Locate every blood parasite and identify its species.
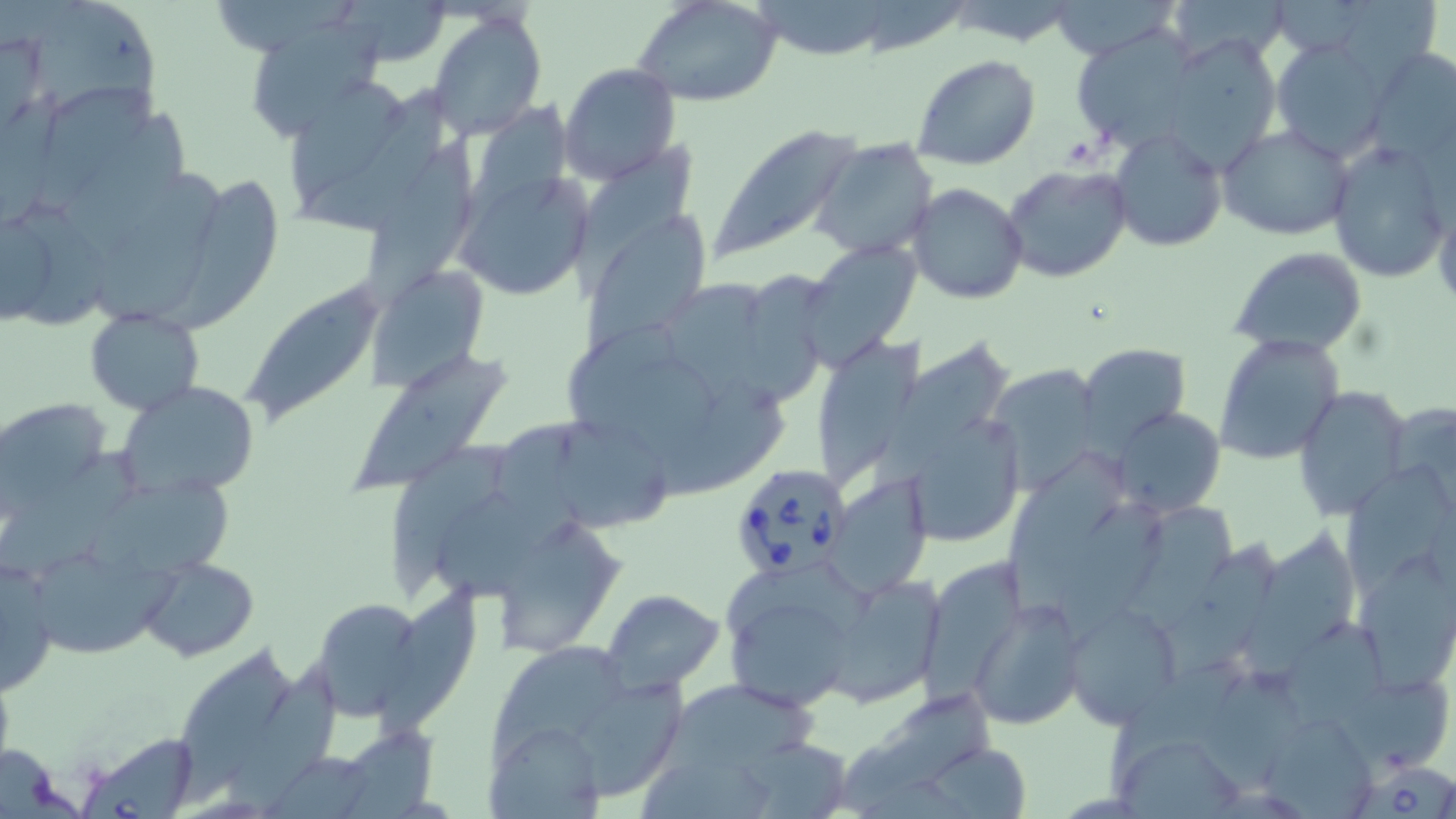
Approximate bounding boxes as named x1/y1/x2/y2 corners in pixels.
Babesia divergens-infected red blood cells: (x1=726, y1=460, x2=856, y2=579), (x1=76, y1=733, x2=201, y2=817), (x1=1354, y1=763, x2=1456, y2=819).
No Plasmodium falciparum, Plasmodium ovale, Plasmodium malariae, Plasmodium vivax, or Trypanosoma brucei observed.

Uninfected red blood cell locations: (x1=342, y1=0, x2=455, y2=68), (x1=1052, y1=0, x2=1176, y2=58), (x1=1164, y1=0, x2=1293, y2=65), (x1=1347, y1=0, x2=1440, y2=91), (x1=758, y1=1, x2=890, y2=65), (x1=1276, y1=1, x2=1370, y2=55), (x1=635, y1=2, x2=784, y2=108), (x1=213, y1=3, x2=365, y2=52), (x1=29, y1=9, x2=169, y2=129), (x1=428, y1=10, x2=546, y2=139), (x1=252, y1=20, x2=394, y2=149), (x1=1070, y1=29, x2=1202, y2=154), (x1=1162, y1=33, x2=1283, y2=173), (x1=1270, y1=37, x2=1392, y2=161), (x1=1366, y1=48, x2=1455, y2=163), (x1=911, y1=54, x2=1040, y2=171), (x1=559, y1=63, x2=682, y2=187), (x1=292, y1=81, x2=410, y2=210), (x1=306, y1=83, x2=456, y2=240), (x1=38, y1=85, x2=168, y2=218), (x1=460, y1=91, x2=583, y2=260), (x1=61, y1=116, x2=196, y2=268), (x1=1110, y1=125, x2=1229, y2=253), (x1=709, y1=126, x2=865, y2=262), (x1=1219, y1=126, x2=1355, y2=240), (x1=358, y1=133, x2=486, y2=317), (x1=565, y1=139, x2=699, y2=308), (x1=810, y1=139, x2=939, y2=260), (x1=1326, y1=141, x2=1451, y2=284), (x1=1001, y1=162, x2=1133, y2=283), (x1=96, y1=166, x2=223, y2=328), (x1=456, y1=167, x2=597, y2=305), (x1=156, y1=176, x2=275, y2=336), (x1=907, y1=182, x2=1029, y2=306), (x1=12, y1=201, x2=111, y2=330), (x1=580, y1=215, x2=711, y2=355), (x1=802, y1=242, x2=920, y2=365), (x1=1230, y1=247, x2=1369, y2=354), (x1=734, y1=255, x2=831, y2=410), (x1=371, y1=266, x2=487, y2=385), (x1=239, y1=273, x2=391, y2=431), (x1=660, y1=276, x2=777, y2=416), (x1=85, y1=308, x2=203, y2=415), (x1=568, y1=320, x2=721, y2=464), (x1=826, y1=327, x2=925, y2=485), (x1=1213, y1=333, x2=1344, y2=464), (x1=868, y1=337, x2=1012, y2=518), (x1=1076, y1=342, x2=1191, y2=452), (x1=349, y1=343, x2=505, y2=490), (x1=983, y1=362, x2=1104, y2=494), (x1=653, y1=380, x2=793, y2=515), (x1=117, y1=382, x2=261, y2=498), (x1=1293, y1=386, x2=1411, y2=521), (x1=3, y1=397, x2=113, y2=507), (x1=1388, y1=399, x2=1456, y2=509), (x1=1112, y1=406, x2=1226, y2=517), (x1=550, y1=412, x2=669, y2=539), (x1=487, y1=416, x2=620, y2=544), (x1=392, y1=443, x2=514, y2=595), (x1=0, y1=446, x2=159, y2=579), (x1=1005, y1=455, x2=1127, y2=613), (x1=1341, y1=468, x2=1453, y2=592), (x1=828, y1=472, x2=931, y2=598), (x1=90, y1=481, x2=239, y2=581), (x1=1063, y1=497, x2=1170, y2=650), (x1=1124, y1=503, x2=1241, y2=645), (x1=497, y1=519, x2=629, y2=655), (x1=1243, y1=528, x2=1358, y2=685), (x1=1166, y1=541, x2=1280, y2=677), (x1=1362, y1=547, x2=1455, y2=692), (x1=1, y1=552, x2=59, y2=698), (x1=35, y1=554, x2=185, y2=657), (x1=919, y1=556, x2=1020, y2=713), (x1=139, y1=558, x2=258, y2=659), (x1=834, y1=580, x2=947, y2=712), (x1=719, y1=581, x2=859, y2=712), (x1=374, y1=584, x2=480, y2=744), (x1=603, y1=589, x2=724, y2=694), (x1=308, y1=596, x2=437, y2=721), (x1=970, y1=598, x2=1086, y2=730), (x1=1060, y1=598, x2=1184, y2=730), (x1=1285, y1=622, x2=1391, y2=730), (x1=178, y1=645, x2=299, y2=802), (x1=491, y1=648, x2=626, y2=770), (x1=231, y1=655, x2=351, y2=812), (x1=1107, y1=655, x2=1254, y2=786), (x1=1198, y1=666, x2=1306, y2=790), (x1=1340, y1=669, x2=1452, y2=782), (x1=655, y1=678, x2=826, y2=779), (x1=555, y1=679, x2=691, y2=807), (x1=832, y1=693, x2=992, y2=817), (x1=1259, y1=710, x2=1378, y2=818), (x1=336, y1=721, x2=444, y2=819), (x1=486, y1=726, x2=602, y2=819), (x1=734, y1=735, x2=856, y2=817), (x1=920, y1=742, x2=1031, y2=817), (x1=1112, y1=742, x2=1247, y2=818), (x1=636, y1=757, x2=782, y2=819). Slide-level diagnosis: Babesia divergens. Light microscopy. May-Grünwald-Giemsa stain. Single field of view. Captured at 1000x magnification. Image is 1456×819 pixels. Thin blood film.